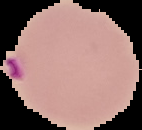

Image is 142×130 pixels. Segmented cell region on a black background. From a thin blood smear. Result: malaria parasites identified.